State the preparation type.
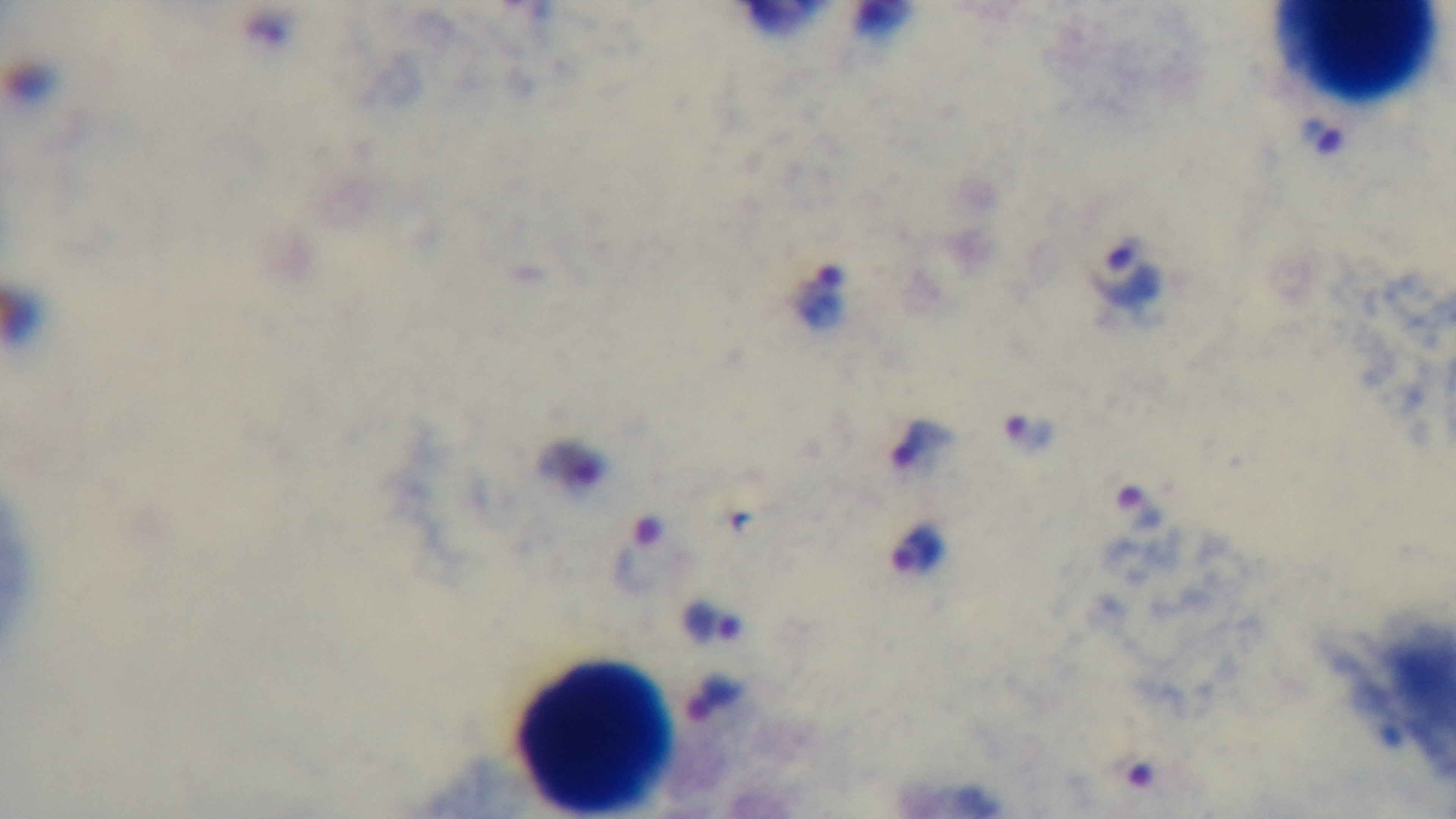
It is a thick blood film.

Summary:
  - Field of view: single
  - Stain: Giemsa
  - Malaria status: positive
  - Modality: light microscopy
  - Capture: mounted 4K digital camera
  - Objective: 100x oil immersion